Assess this cell for malaria.
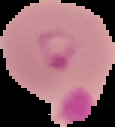
Parasitized.

Image is 115×127 pixels. From a thin blood smear. The area outside the segmented cell region is set to black.